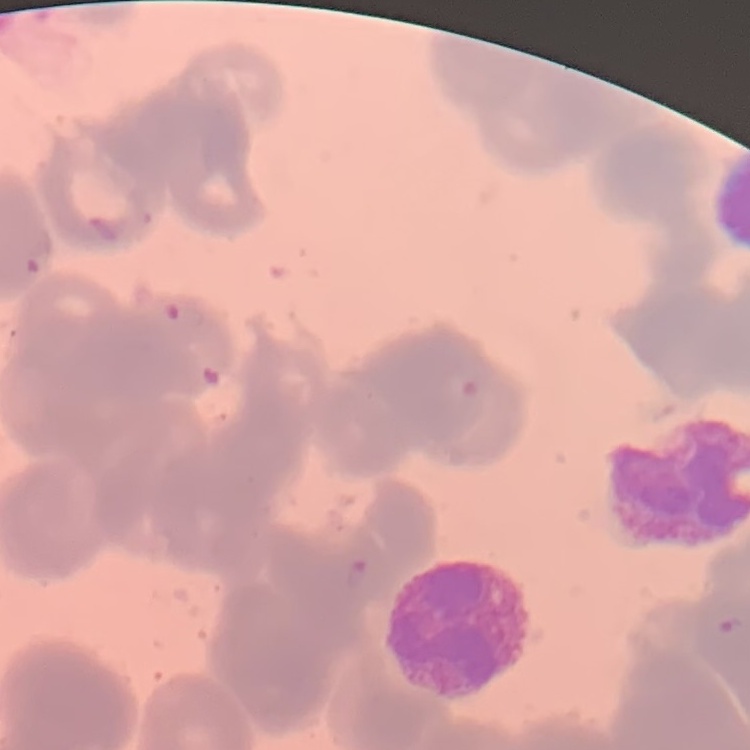
{
  "erythrocyte_morphology": "rouleaux formation",
  "stain": "Field's or Giemsa",
  "preparation": "thin blood smear",
  "image_type": "one tile cut from a larger photomicrograph"
}